Assess this cell for malaria.
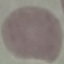

It is uninfected.

stain = Giemsa
preparation = thin blood smear
capture = smartphone through the microscope eyepiece
image type = cell patch, automatically extracted from a larger field of view and resized to 64 × 64 pixels